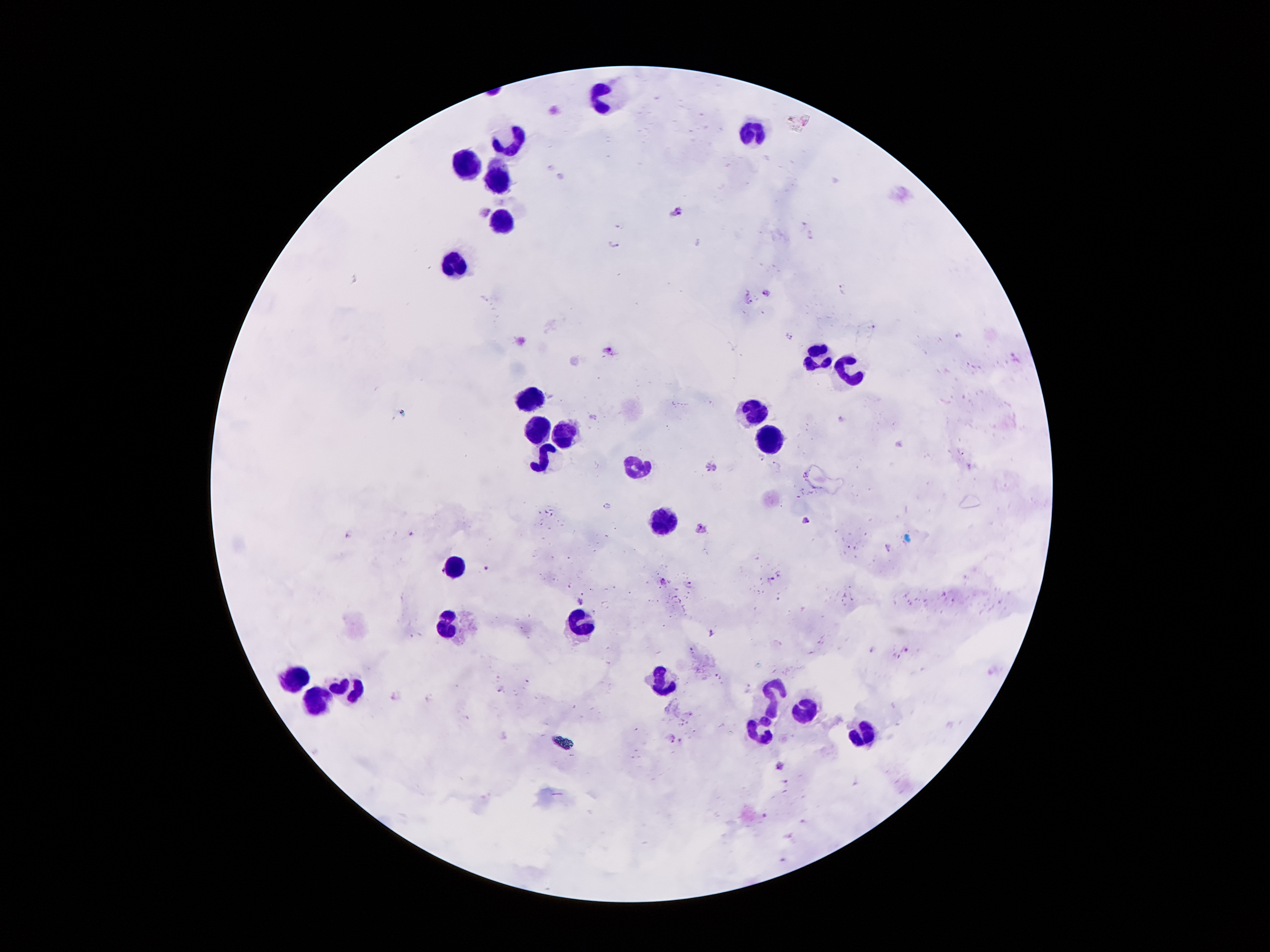

coordinate format = approximate centers as (x, y) in pixels
leukocyte locations = (605, 94), (756, 129), (513, 142), (467, 164), (494, 178), (502, 220), (456, 265), (819, 354), (849, 370), (528, 399), (756, 411), (538, 428), (563, 430), (767, 441), (544, 458), (641, 465), (664, 521), (456, 568), (584, 622), (452, 626), (292, 676), (662, 680), (353, 687), (769, 691), (320, 699), (802, 713), (756, 731), (859, 732)
malaria parasite locations = (485, 211), (675, 211), (812, 235), (615, 246), (842, 288), (768, 293), (748, 297), (959, 333), (791, 335), (609, 350), (711, 466), (805, 521), (700, 525), (409, 534), (349, 535), (488, 568), (779, 573), (662, 580), (769, 580), (690, 583), (581, 602), (712, 632), (905, 648), (500, 687), (672, 736), (780, 766), (786, 783), (762, 814), (804, 821), (790, 837)
capture = smartphone through the microscope eyepiece
stain = Giemsa
magnification = 100x
patient malaria status = infected with Plasmodium falciparum
field of view = one from this slide
image size = 1270×952 pixels
preparation = thick peripheral-blood smear